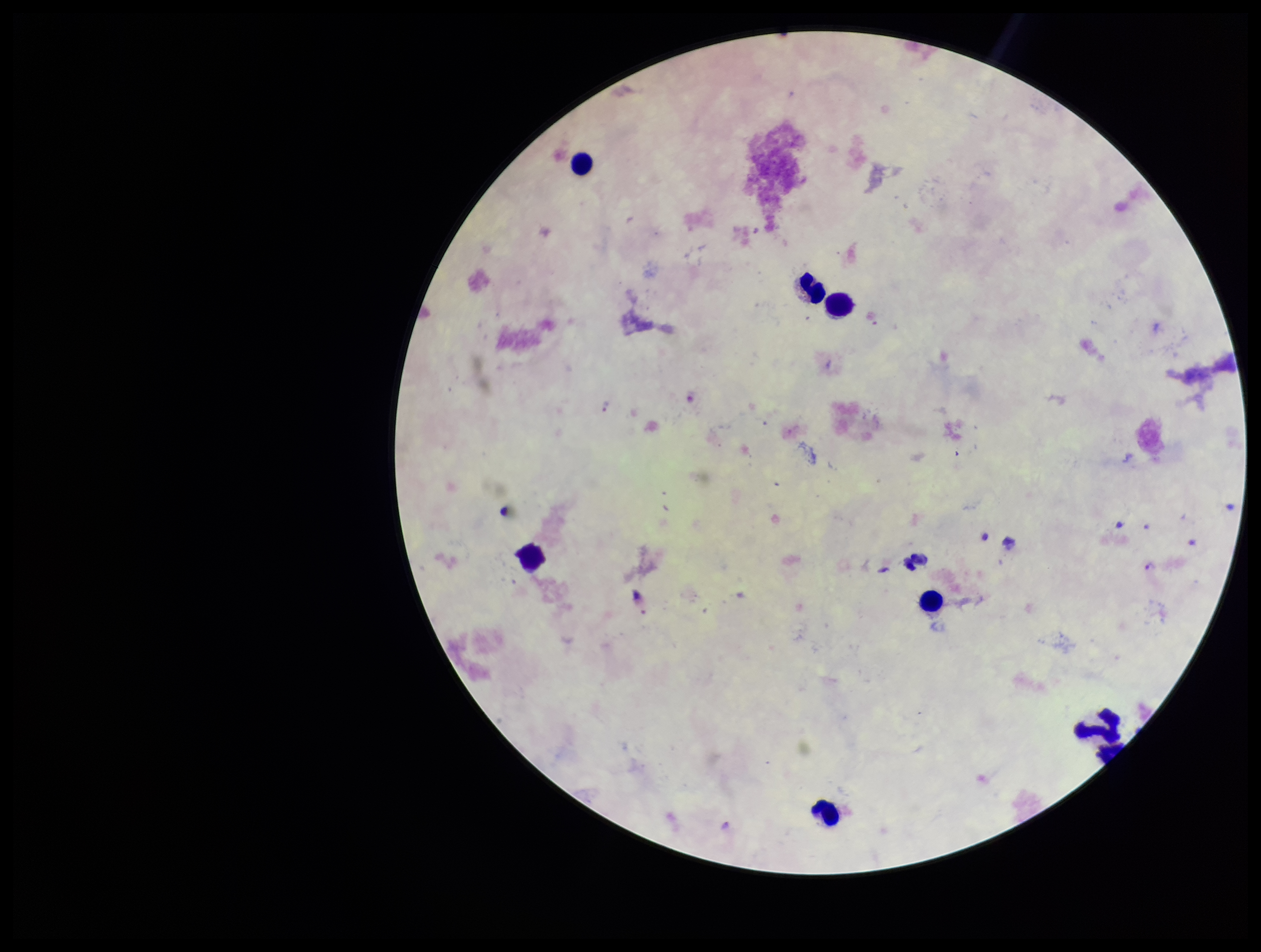
species reported for this patient = Plasmodium falciparum
capture = smartphone photograph through the microscope eyepiece
leukocyte count = 7
Plasmodium parasites = seen
image size = 1261×952 pixels
patient malaria status = positive
preparation = thick blood smear
parasite count = 2
field of view = one from this slide
stain = Giemsa